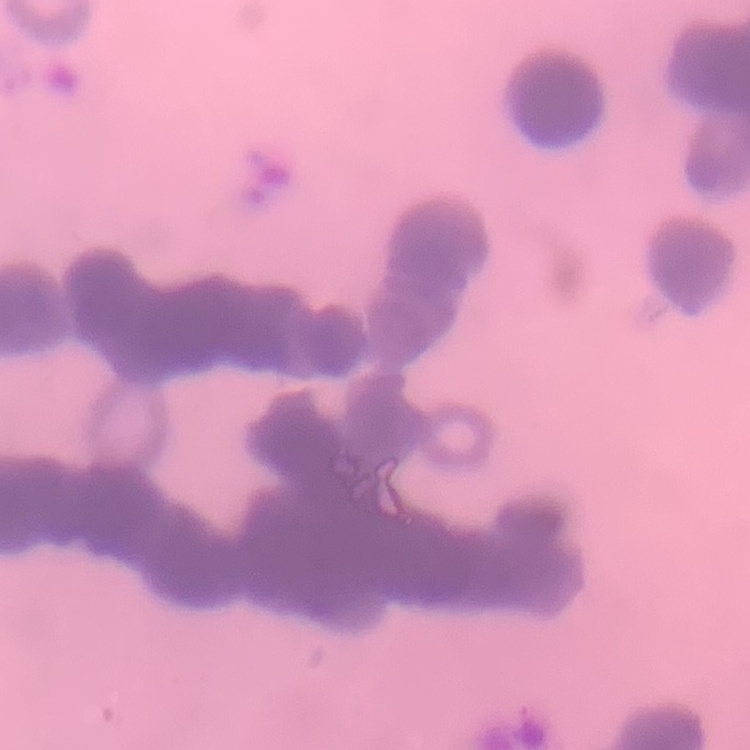

The red blood cells exhibit rouleaux formation. One tile cut from a larger photomicrograph. Field's or Giemsa stain. Thin blood smear.